Assess for malaria.
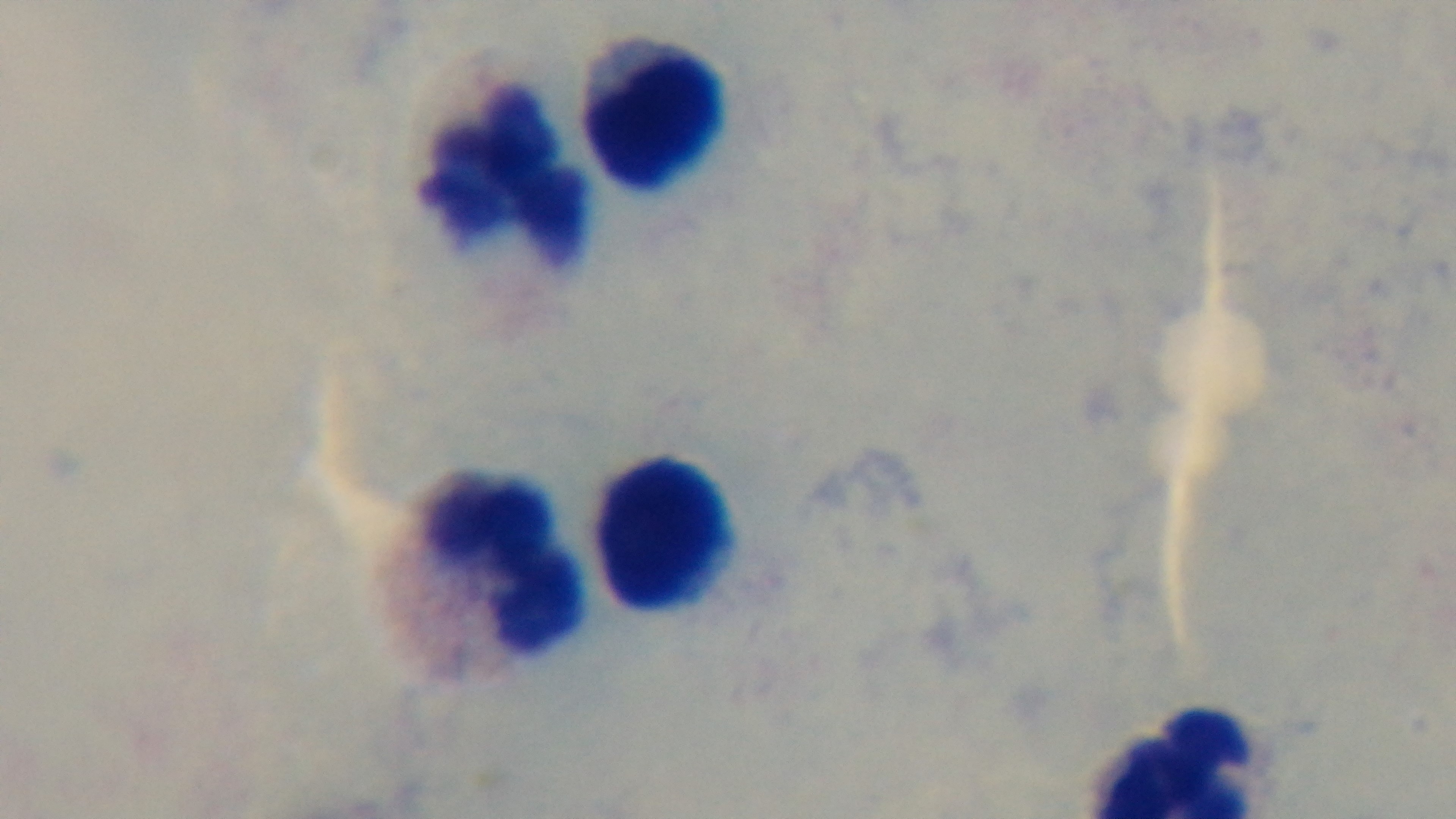

It is uninfected.

Mounted 4K digital camera. Preparation: thick. One field from the slide. Giemsa stain. Photomicrograph. Oil-immersion objective, 100x.